Name the parasite shown.
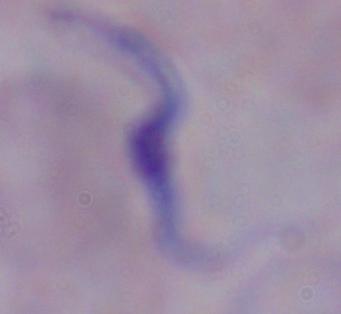
This is a trypanosome.

Photomicrograph. Captured at 1000x magnification.